Identify the parasite.
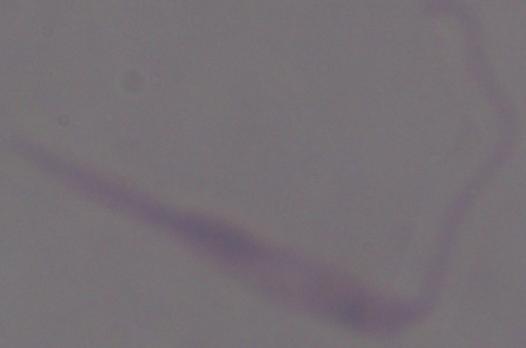
This is Leishmania.

Summary:
  - Magnification: 1000x
  - Modality: photomicrograph